Assess the morphology of the erythrocytes.
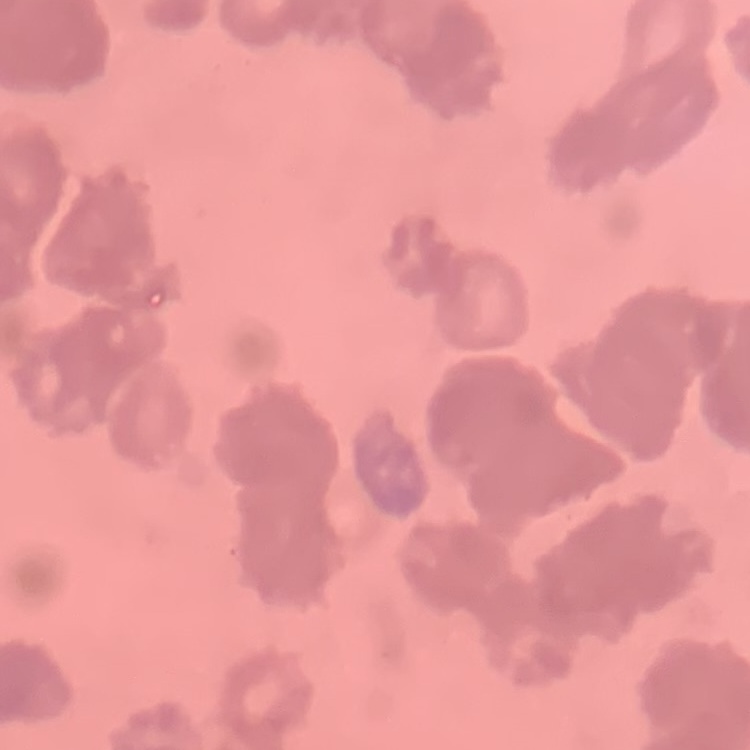
They show rouleaux formation.

Summary:
  - Stain: Field's or Giemsa
  - Image type: one tile cut from a larger photomicrograph
  - Preparation: thin peripheral smear